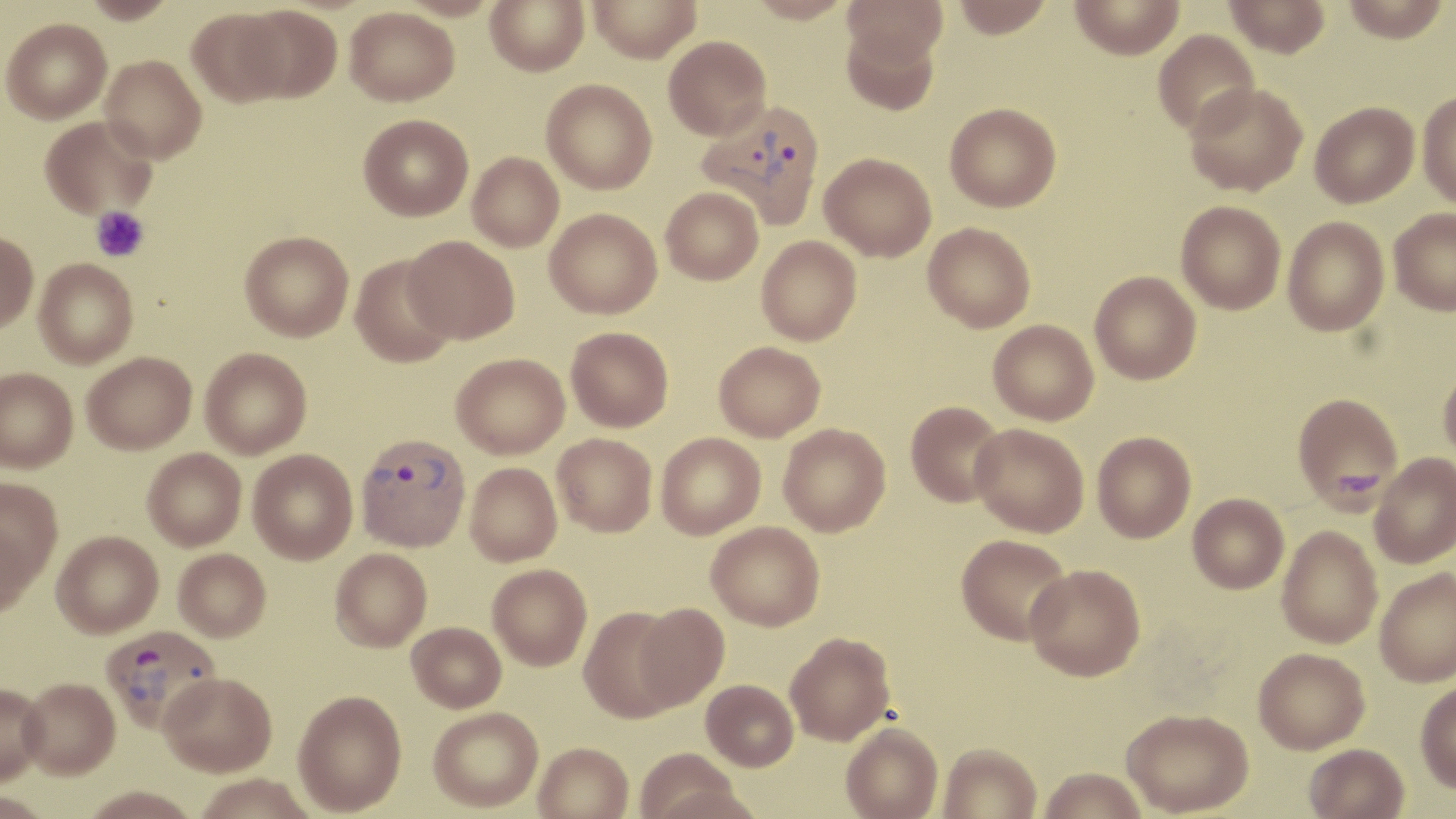

{
  "slide_level_diagnosis": "Plasmodium vivax",
  "stain": "May-Grünwald-Giemsa",
  "magnification": "1000x",
  "image_size": "1456×819 pixels",
  "modality": "optical microscopy",
  "field_of_view": "single",
  "uninfected_red_blood_cell_locations": "approximate bounding boxes as named x1/y1/x2/y2 corners in pixels: (x1=81, y1=0, x2=179, y2=24), (x1=485, y1=0, x2=589, y2=76), (x1=588, y1=0, x2=702, y2=63), (x1=744, y1=0, x2=854, y2=24), (x1=843, y1=0, x2=947, y2=65), (x1=951, y1=0, x2=1054, y2=39), (x1=1069, y1=0, x2=1185, y2=60), (x1=1223, y1=0, x2=1330, y2=58), (x1=1341, y1=0, x2=1451, y2=42), (x1=235, y1=5, x2=343, y2=103), (x1=344, y1=6, x2=459, y2=106), (x1=186, y1=7, x2=291, y2=106), (x1=1, y1=18, x2=112, y2=123), (x1=839, y1=20, x2=941, y2=115), (x1=1153, y1=30, x2=1260, y2=137), (x1=663, y1=35, x2=771, y2=140), (x1=100, y1=55, x2=207, y2=163), (x1=541, y1=78, x2=657, y2=194), (x1=1185, y1=81, x2=1308, y2=196), (x1=1417, y1=91, x2=1456, y2=208), (x1=945, y1=102, x2=1061, y2=212), (x1=1310, y1=102, x2=1419, y2=208), (x1=358, y1=114, x2=473, y2=221), (x1=40, y1=116, x2=156, y2=220), (x1=467, y1=152, x2=563, y2=251), (x1=820, y1=152, x2=936, y2=261), (x1=661, y1=186, x2=764, y2=285), (x1=1176, y1=200, x2=1286, y2=314), (x1=1389, y1=207, x2=1456, y2=315), (x1=544, y1=208, x2=662, y2=318), (x1=1282, y1=216, x2=1389, y2=336), (x1=923, y1=222, x2=1036, y2=332), (x1=240, y1=230, x2=354, y2=341), (x1=0, y1=231, x2=39, y2=333), (x1=404, y1=235, x2=520, y2=343), (x1=756, y1=236, x2=861, y2=345), (x1=349, y1=254, x2=458, y2=368), (x1=34, y1=258, x2=138, y2=368), (x1=1090, y1=271, x2=1201, y2=384), (x1=988, y1=320, x2=1099, y2=425), (x1=566, y1=326, x2=674, y2=432), (x1=714, y1=341, x2=825, y2=441), (x1=199, y1=347, x2=312, y2=458), (x1=82, y1=351, x2=197, y2=454), (x1=451, y1=353, x2=569, y2=458), (x1=1438, y1=365, x2=1456, y2=465), (x1=0, y1=368, x2=78, y2=473), (x1=1292, y1=392, x2=1404, y2=511), (x1=905, y1=400, x2=1007, y2=507), (x1=970, y1=422, x2=1089, y2=537), (x1=778, y1=423, x2=891, y2=536), (x1=1092, y1=431, x2=1196, y2=543), (x1=656, y1=432, x2=765, y2=539), (x1=552, y1=433, x2=657, y2=536), (x1=142, y1=448, x2=246, y2=551), (x1=248, y1=449, x2=358, y2=564), (x1=1370, y1=452, x2=1456, y2=568), (x1=465, y1=462, x2=562, y2=566), (x1=0, y1=478, x2=63, y2=588), (x1=1187, y1=493, x2=1289, y2=593), (x1=706, y1=521, x2=825, y2=630), (x1=0, y1=522, x2=38, y2=616), (x1=1277, y1=526, x2=1383, y2=649), (x1=51, y1=530, x2=163, y2=638), (x1=956, y1=533, x2=1073, y2=645), (x1=173, y1=548, x2=271, y2=642), (x1=330, y1=548, x2=432, y2=651), (x1=487, y1=563, x2=592, y2=670), (x1=1025, y1=563, x2=1146, y2=681), (x1=1374, y1=568, x2=1456, y2=686), (x1=634, y1=603, x2=730, y2=711), (x1=579, y1=606, x2=685, y2=722), (x1=406, y1=621, x2=506, y2=713), (x1=785, y1=631, x2=895, y2=745), (x1=1253, y1=648, x2=1369, y2=754), (x1=160, y1=673, x2=276, y2=779), (x1=701, y1=679, x2=798, y2=771), (x1=19, y1=680, x2=120, y2=782), (x1=1415, y1=681, x2=1456, y2=793), (x1=0, y1=685, x2=49, y2=788), (x1=293, y1=690, x2=407, y2=816), (x1=428, y1=707, x2=543, y2=813), (x1=1122, y1=708, x2=1253, y2=816), (x1=841, y1=722, x2=943, y2=819), (x1=937, y1=742, x2=1041, y2=819), (x1=533, y1=743, x2=633, y2=819), (x1=1303, y1=744, x2=1408, y2=819), (x1=633, y1=748, x2=745, y2=819), (x1=1039, y1=767, x2=1147, y2=819), (x1=195, y1=774, x2=317, y2=819), (x1=82, y1=787, x2=199, y2=819), (x1=0, y1=793, x2=50, y2=819)",
  "preparation": "thin blood film",
  "plasmodium_vivax_infected_red_blood_cell_locations": "approximate bounding boxes as named x1/y1/x2/y2 corners in pixels: (x1=697, y1=100, x2=826, y2=228), (x1=355, y1=432, x2=471, y2=552), (x1=100, y1=624, x2=221, y2=735)",
  "platelet_locations": "approximate bounding boxes as named x1/y1/x2/y2 corners in pixels: (x1=91, y1=206, x2=149, y2=263)"
}